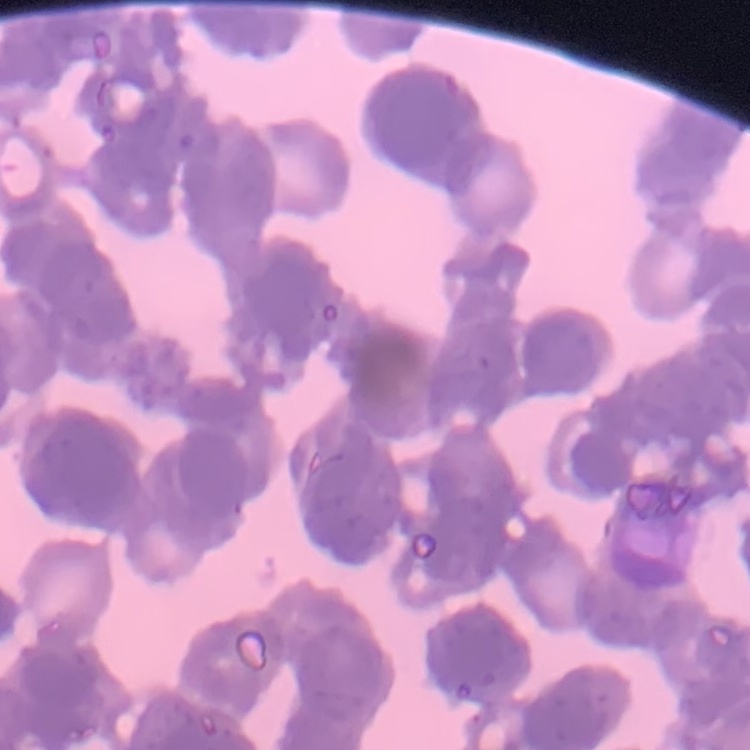
Summary:
  - Erythrocyte morphology: rouleaux formation
  - Preparation: thin blood smear
  - Image type: one tile cut from a larger photomicrograph
  - Stain: Field's or Giemsa